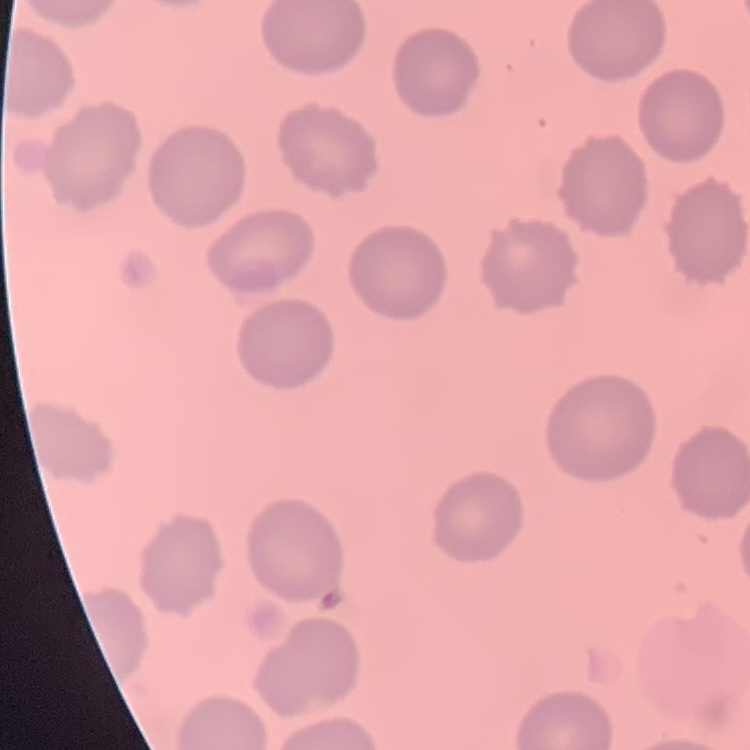 The red blood cells show no rouleaux formation. Field's or Giemsa stain. Square crop of a larger photomicrograph. Thin peripheral smear.